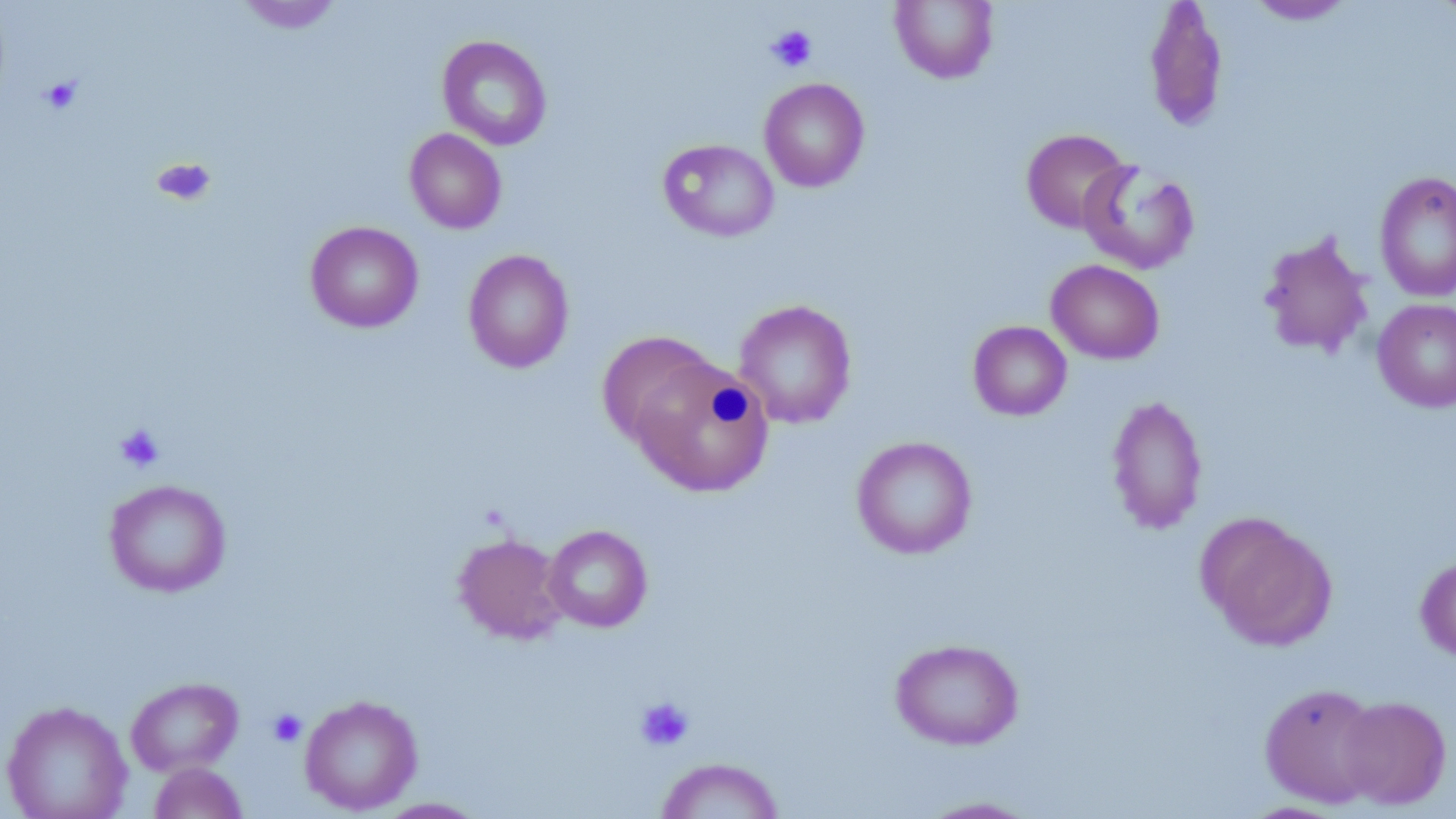
{
  "slide_level_diagnosis": "no evidence of blood parasites",
  "platelet_locations": "approximate bounding boxes as (x1, y1, x2, y2) in pixels: (766, 25, 817, 72), (39, 76, 83, 114), (153, 157, 216, 205), (114, 424, 165, 473), (635, 697, 694, 751), (267, 708, 306, 748)",
  "modality": "light microscopy",
  "field_of_view": "one of a larger specimen",
  "image_size": "1456×819 pixels",
  "stain": "May-Grünwald-Giemsa",
  "preparation": "thin blood smear",
  "uninfected_red_blood_cell_locations": "approximate bounding boxes as (x1, y1, x2, y2) in pixels: (235, 0, 344, 34), (890, 0, 999, 84), (1143, 0, 1229, 134), (1244, 0, 1355, 25), (437, 35, 553, 150), (759, 77, 870, 192), (404, 128, 507, 234), (1021, 128, 1131, 234), (658, 139, 779, 242), (1078, 159, 1200, 274), (1374, 170, 1456, 303), (305, 220, 424, 333), (1257, 231, 1375, 360), (463, 249, 575, 373), (1046, 259, 1165, 364), (1372, 298, 1456, 412), (733, 299, 857, 429), (968, 321, 1072, 421), (597, 330, 720, 449), (629, 355, 775, 497), (1106, 394, 1208, 535), (851, 435, 978, 559), (104, 479, 232, 598), (1199, 513, 1337, 651), (543, 524, 652, 632), (453, 532, 568, 645), (1415, 554, 1456, 662), (890, 637, 1024, 750), (125, 676, 244, 777), (1259, 683, 1384, 808), (299, 694, 423, 815), (1338, 696, 1452, 810), (0, 699, 133, 819), (655, 756, 784, 818), (148, 762, 248, 819), (914, 796, 1046, 818), (374, 797, 488, 818)",
  "magnification": "1000x"
}